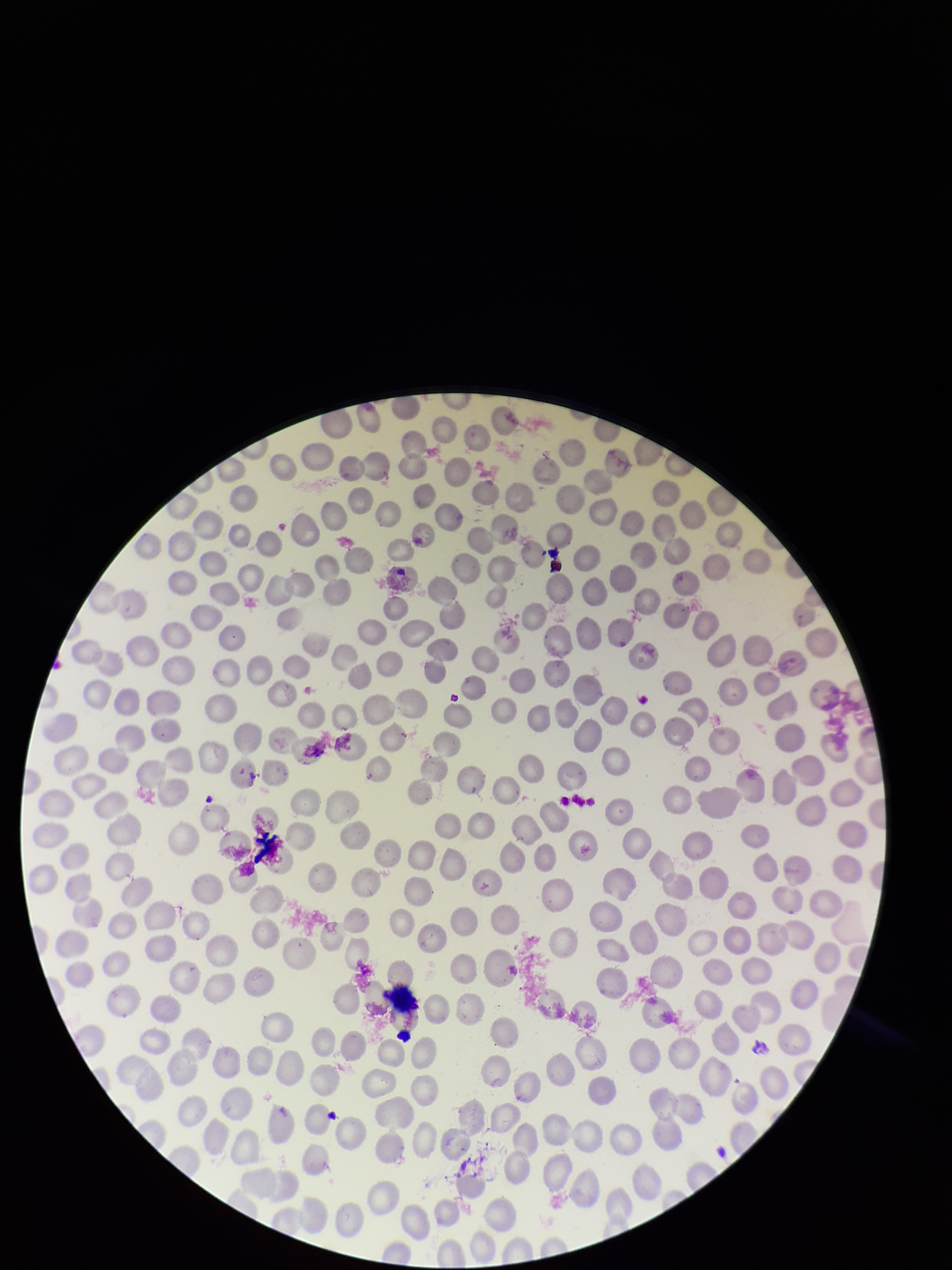

Summary:
  - Capture: smartphone photograph through the microscope eyepiece
  - Image size: 952×1270 pixels
  - Preparation: thin
  - Field of view: single
  - Parasitized red blood cell count: 0
  - Red blood cell count: 251
  - Stain: Giemsa
  - Parasitized red blood cells: none identified
  - Patient malaria status: negative